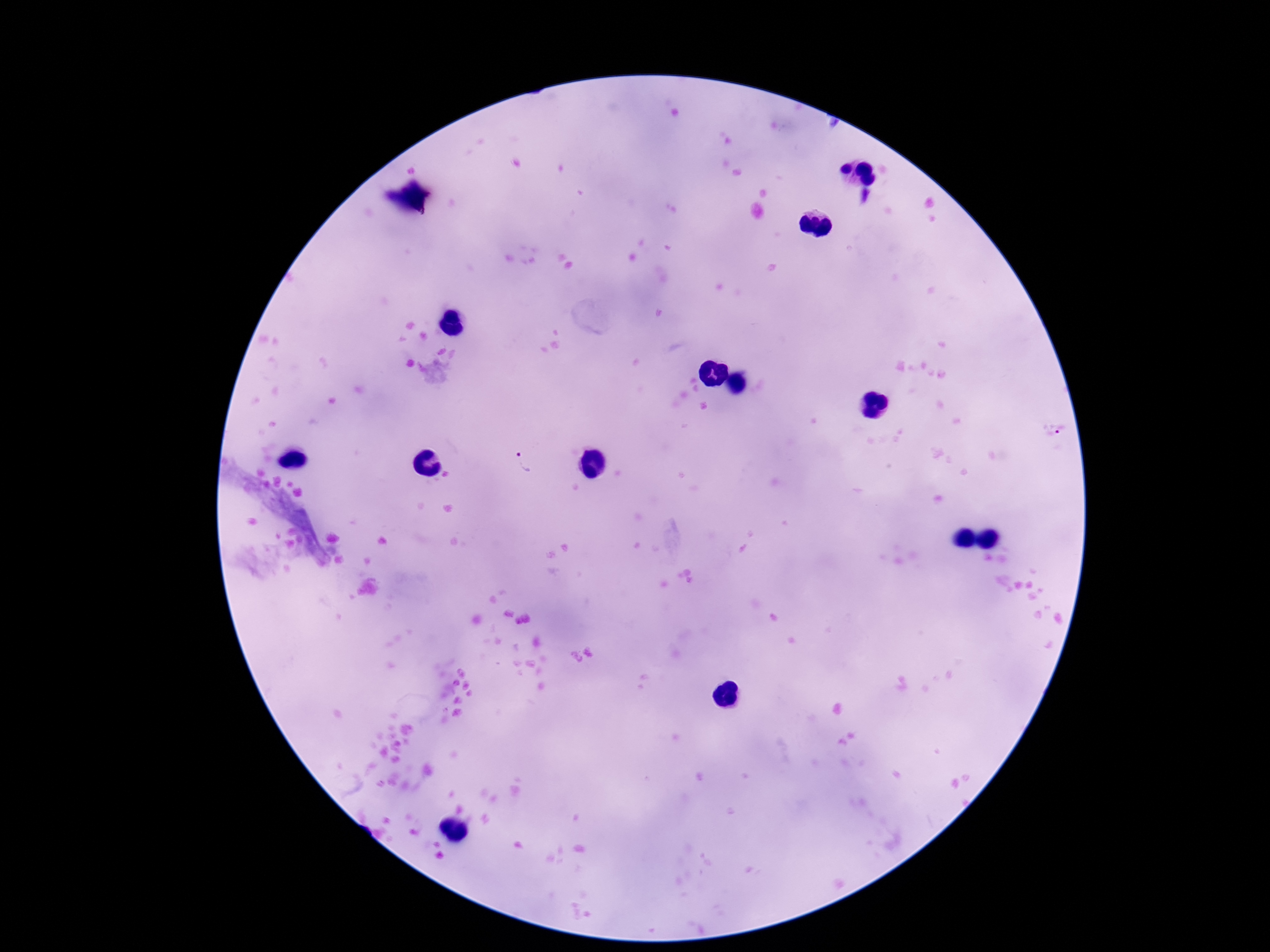 Approximate centers as (x, y) in pixels. Plasmodium parasite locations: (1056, 429), (522, 465). Thick peripheral-blood smear. Giemsa-stained preparation. Single field of view. Patient malaria status: infected. Image is 1270×952 pixels. Smartphone photograph taken through the microscope eyepiece. 100x magnification.